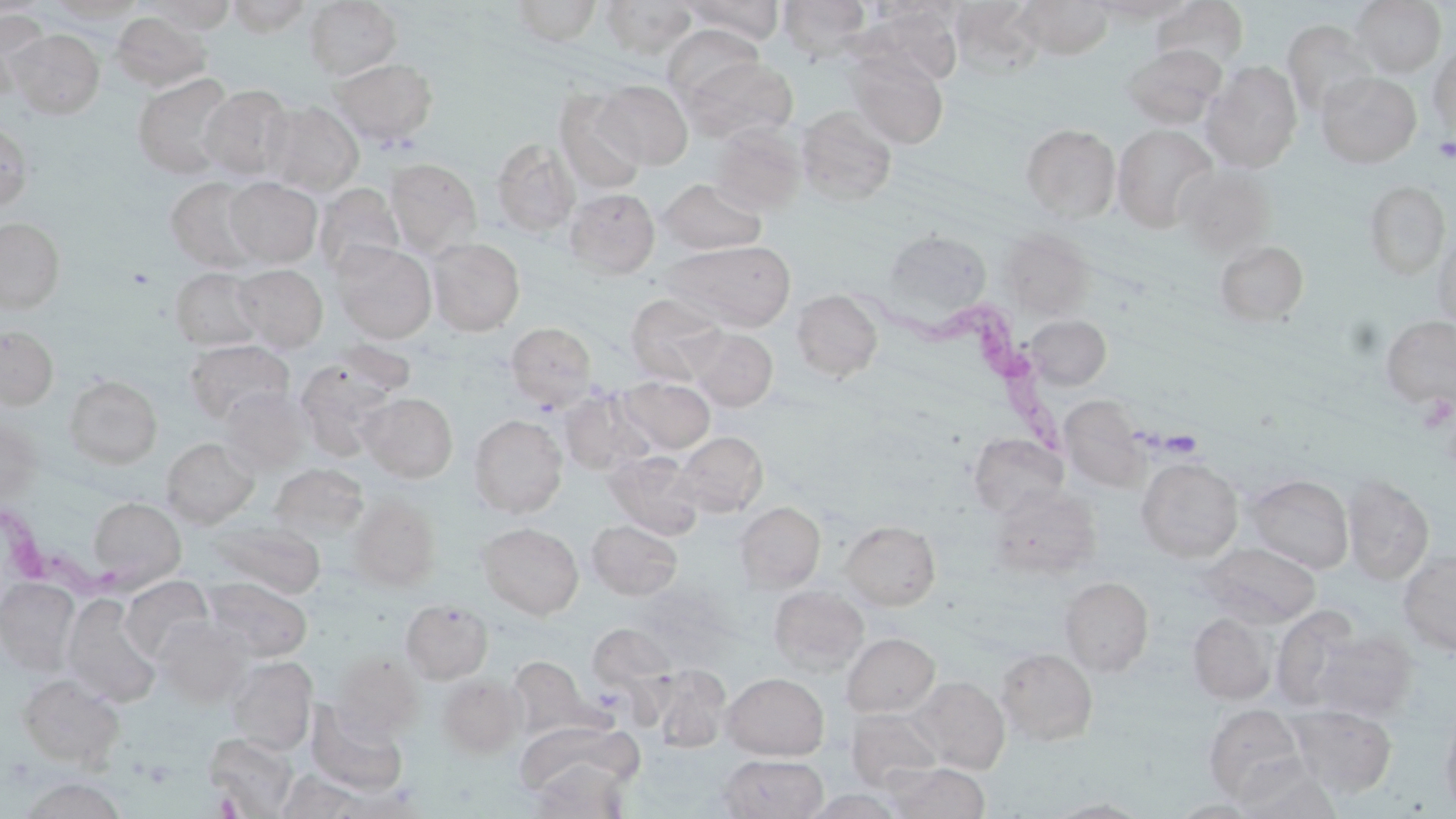

Summary:
  - Coordinate format: approximate bounding boxes as (x1,y1)-(x2,y2) corner pairs in pixels
  - Platelet locations: (1434,136)-(1456,164), (213,793)-(244,817)
  - Uninfected red blood cell locations: (226,0)-(313,36), (601,0)-(697,59), (684,0)-(784,45), (778,0)-(872,60), (1017,0)-(1112,59), (1091,0)-(1192,23), (1349,0)-(1446,78), (46,1)-(147,23), (145,1)-(236,32), (304,1)-(402,79), (507,1)-(603,46), (862,1)-(967,24), (1153,1)-(1248,72), (857,5)-(964,86), (0,8)-(49,87), (111,12)-(211,92), (1283,20)-(1378,118), (662,24)-(763,104), (6,29)-(105,118), (1428,42)-(1456,136), (1123,44)-(1226,129), (848,53)-(949,149), (682,56)-(798,143), (331,59)-(437,144), (1202,62)-(1302,172), (1316,72)-(1421,168), (132,74)-(235,179), (595,81)-(693,169), (199,84)-(295,181), (554,91)-(648,195), (262,100)-(363,195), (796,106)-(897,206), (0,119)-(33,209), (710,124)-(806,215), (1021,124)-(1121,222), (1112,124)-(1218,233), (491,138)-(580,236), (385,159)-(481,255), (1175,165)-(1275,257), (166,178)-(266,273), (225,178)-(322,267), (658,178)-(766,255), (1364,180)-(1450,281), (315,183)-(404,278), (565,188)-(659,277), (0,218)-(65,313), (1432,227)-(1456,329), (1001,228)-(1094,318), (882,229)-(991,325), (426,237)-(525,336), (1215,239)-(1309,327), (666,240)-(796,331), (332,242)-(436,342), (232,264)-(328,352), (169,267)-(263,351), (791,289)-(882,381), (625,293)-(727,384), (1025,315)-(1111,390), (1381,315)-(1456,408), (506,322)-(597,411), (0,326)-(59,409), (686,328)-(778,411), (184,339)-(294,425), (294,352)-(407,459), (64,375)-(163,468), (617,376)-(715,453), (558,386)-(658,477), (218,388)-(312,473), (358,392)-(457,482), (1060,395)-(1149,492), (469,414)-(568,517), (0,419)-(43,503), (675,431)-(768,516), (968,433)-(1068,517), (162,437)-(259,528), (604,451)-(705,539), (1136,457)-(1243,561), (269,464)-(369,543), (1245,474)-(1354,573), (1342,474)-(1434,585), (990,485)-(1101,578), (348,495)-(441,590), (88,497)-(186,589), (735,501)-(825,592), (586,519)-(682,600), (211,520)-(325,597), (841,520)-(940,610), (477,522)-(584,619), (1202,542)-(1320,628), (1398,550)-(1456,656), (119,576)-(213,663), (202,577)-(312,661), (1059,577)-(1154,676), (0,578)-(80,673), (769,585)-(869,675), (62,595)-(161,707), (401,598)-(493,683), (1271,607)-(1362,710), (1188,612)-(1276,704), (153,617)-(252,706), (587,624)-(677,697), (1313,630)-(1417,722), (841,633)-(939,717), (996,648)-(1098,745), (332,651)-(422,739), (508,656)-(591,738), (224,657)-(318,753), (651,666)-(731,752), (19,673)-(125,769), (437,673)-(525,757), (723,673)-(829,760), (912,676)-(1010,774), (306,703)-(408,795), (1204,704)-(1307,803), (1287,705)-(1397,796), (1440,707)-(1456,814), (846,709)-(943,792), (519,715)-(652,790), (203,733)-(298,817), (718,754)-(827,818), (526,759)-(633,817), (1228,761)-(1343,818), (883,762)-(990,818), (275,770)-(367,818), (18,777)-(128,819), (801,789)-(905,818), (1047,798)-(1152,818), (1172,799)-(1260,818)
  - Trypanosoma brucei locations: (854,279)-(1077,464), (1,503)-(142,605)
  - Slide-level diagnosis: Trypanosoma brucei
  - Preparation: thin blood film
  - Image size: 1456×819 pixels
  - Stain: May-Grünwald-Giemsa
  - Modality: light microscopy
  - Magnification: 1000x
  - Field of view: one of a larger specimen